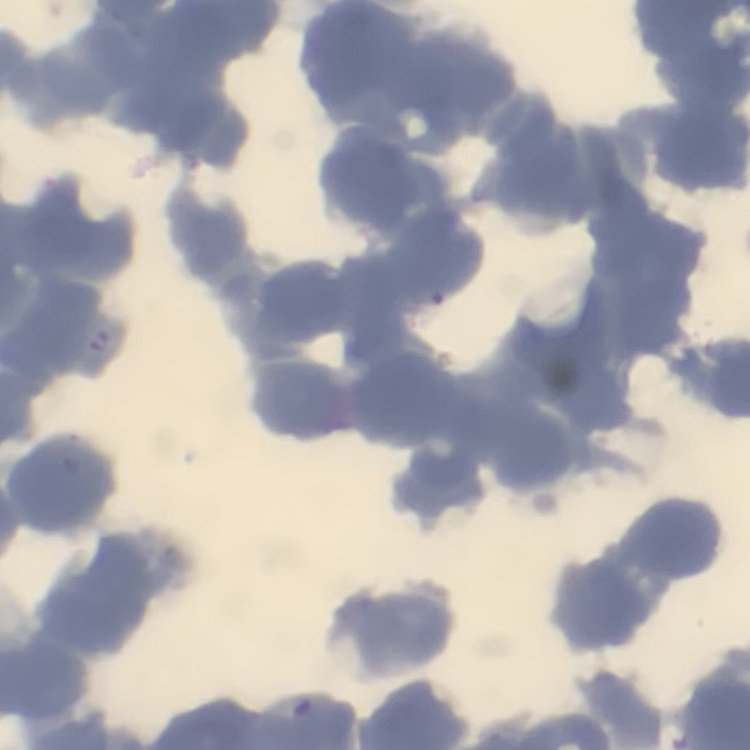
{
  "erythrocyte_morphology": "rouleaux formation",
  "image_type": "one tile cut from a larger photomicrograph",
  "stain": "Field's or Giemsa",
  "preparation": "thin blood smear"
}